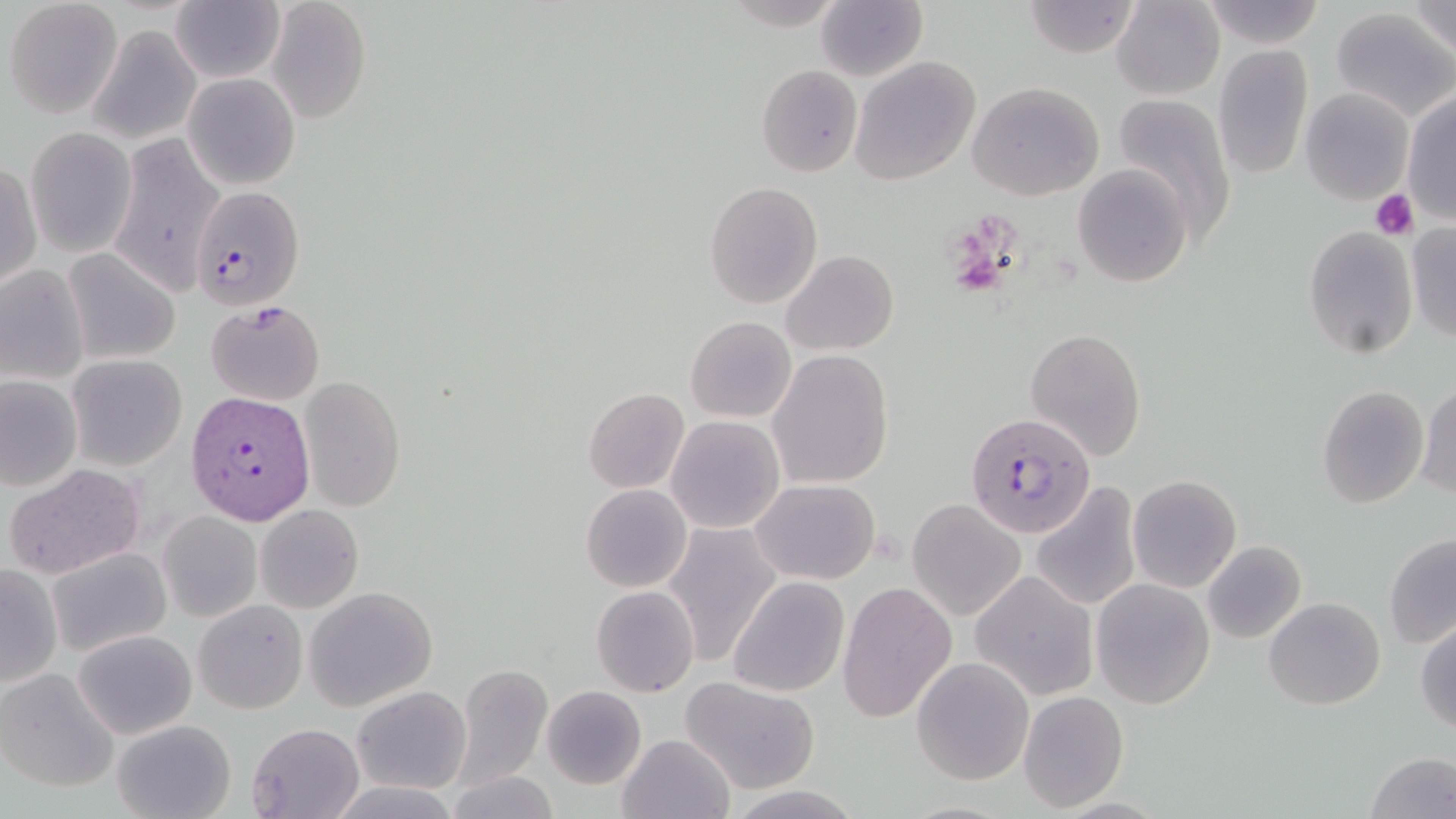

slide_level_diagnosis: Plasmodium falciparum
field_of_view: one of a larger specimen
platelet_locations: 'approximate bounding boxes as [x1, y1, x2, y2] in pixels: [1371, 190, 1419, 240]'
preparation: thin blood film
stain: May-Grünwald-Giemsa
modality: optical microscopy
magnification: 1000x
image_size: 1456×819 pixels
uninfected_red_blood_cell_locations: 'approximate bounding boxes as [x1, y1, x2, y2] in pixels: [1113, 0, 1225, 100], [4, 1, 122, 118], [170, 1, 284, 85], [267, 1, 372, 125], [816, 1, 927, 82], [1200, 1, 1327, 49], [1409, 1, 1456, 59], [1021, 2, 1144, 57], [1330, 8, 1456, 125], [90, 24, 204, 144], [1213, 44, 1314, 179], [214, 48, 354, 183], [849, 56, 981, 185], [757, 65, 863, 176], [182, 73, 300, 190], [968, 83, 1104, 202], [1301, 86, 1413, 203], [1402, 93, 1456, 224], [1114, 94, 1237, 238], [26, 127, 136, 255], [110, 134, 223, 299], [2, 161, 41, 293], [1071, 165, 1191, 290], [703, 182, 825, 309], [1406, 224, 1455, 343], [1303, 226, 1417, 357], [63, 249, 180, 364], [781, 249, 900, 356], [0, 264, 90, 384], [204, 301, 326, 404], [685, 316, 797, 423], [1023, 327, 1147, 460], [767, 350, 895, 488], [67, 354, 186, 470], [1, 375, 82, 491], [301, 376, 407, 512], [1416, 383, 1456, 500], [1317, 384, 1429, 510], [581, 387, 690, 494], [665, 414, 785, 534], [4, 465, 145, 578], [1127, 474, 1242, 593], [750, 479, 878, 585], [1030, 482, 1143, 612], [581, 484, 692, 593], [907, 498, 1027, 621], [256, 505, 363, 612], [158, 511, 262, 622], [661, 521, 782, 667], [1383, 533, 1456, 648], [1202, 541, 1307, 643], [47, 546, 172, 656], [0, 565, 62, 687], [969, 569, 1099, 702], [728, 577, 849, 697], [1089, 579, 1216, 709], [837, 582, 957, 726], [304, 586, 438, 712], [591, 586, 700, 697], [1264, 596, 1384, 710], [194, 600, 307, 714], [1415, 619, 1456, 733], [72, 628, 198, 740], [912, 657, 1035, 786], [453, 664, 552, 788], [0, 668, 119, 793], [680, 678, 821, 794], [353, 686, 471, 795], [542, 686, 647, 788], [1017, 691, 1129, 812], [111, 719, 237, 819], [247, 722, 364, 818], [616, 732, 735, 819], [1366, 752, 1456, 819], [447, 770, 559, 819], [331, 777, 457, 817], [721, 784, 864, 819]'
plasmodium_falciparum_infected_red_blood_cell_locations: 'approximate bounding boxes as [x1, y1, x2, y2] in pixels: [190, 184, 305, 312], [185, 391, 316, 526], [965, 412, 1096, 537]'